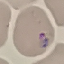
Result: malaria parasites identified. Thin blood film. Giemsa-stained preparation. Automatically extracted cell patch, resized to 64 × 64 pixels. Photographed with a smartphone camera at the microscope eyepiece.